Assess for malaria.
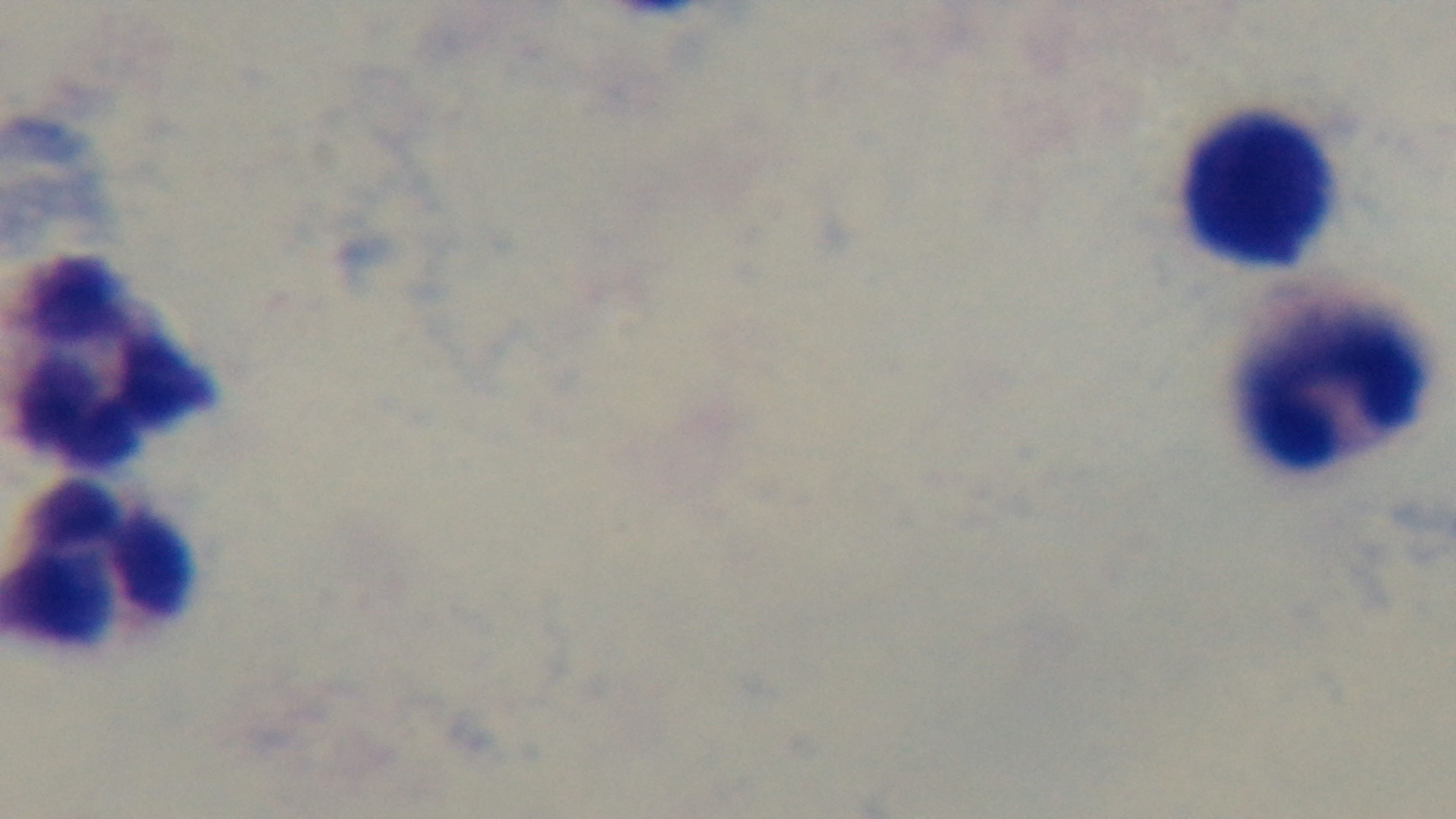
Uninfected.

Summary:
  - Field of view: single
  - Stain: Giemsa
  - Preparation: thick smear
  - Objective: 100x oil immersion
  - Capture: mounted 4K digital camera
  - Modality: light microscopy